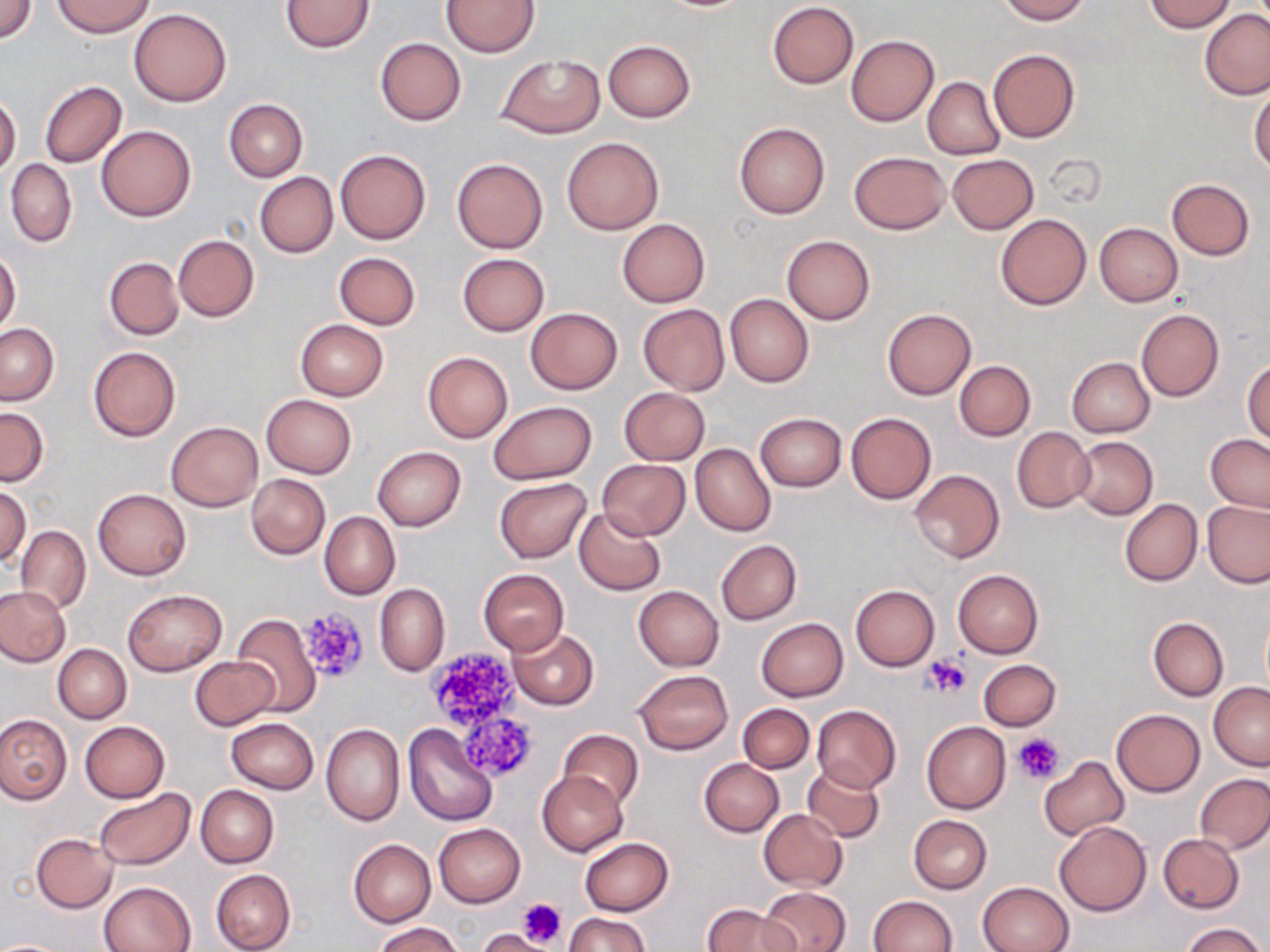

Approximate bounding boxes as (x1,y1)-(x2,y2) corner pairs in pixels. Uninfected red blood cell locations: (51,0)-(153,37), (280,0)-(376,53), (443,0)-(540,57), (998,0)-(1090,23), (1146,0)-(1234,32), (1,1)-(37,42), (768,2)-(858,88), (129,8)-(232,106), (1199,10)-(1270,100), (846,35)-(938,125), (375,38)-(465,125), (603,40)-(696,122), (988,49)-(1080,142), (496,54)-(605,137), (923,77)-(1005,160), (40,82)-(127,168), (1250,86)-(1269,178), (0,95)-(21,176), (224,98)-(308,182), (734,121)-(830,219), (96,125)-(195,221), (561,137)-(663,234), (336,148)-(431,244), (850,151)-(948,233), (947,154)-(1038,234), (451,158)-(548,254), (5,159)-(77,248), (254,172)-(338,258), (1167,179)-(1255,260), (995,212)-(1092,310), (617,219)-(710,308), (1094,223)-(1184,306), (172,234)-(260,322), (782,236)-(875,325), (0,250)-(21,335), (334,252)-(420,330), (457,253)-(549,335), (104,257)-(184,340), (724,293)-(814,387), (638,304)-(729,394), (526,307)-(622,395), (883,308)-(976,399), (1135,308)-(1224,402), (295,319)-(389,401), (0,323)-(58,405), (88,346)-(180,441), (423,351)-(513,443), (1067,357)-(1155,437), (1244,360)-(1270,445), (954,361)-(1035,441), (620,387)-(709,465), (613,389)-(699,539), (260,394)-(357,478), (490,400)-(597,483), (0,407)-(49,485), (755,412)-(846,491), (846,412)-(936,503), (166,421)-(262,511), (1011,428)-(1094,512), (1205,433)-(1270,512), (1071,436)-(1157,519), (690,443)-(776,536), (372,447)-(466,531), (596,458)-(691,540), (909,469)-(1004,564), (246,473)-(329,559), (495,477)-(592,562), (0,486)-(31,569), (93,489)-(191,580), (1119,499)-(1202,587), (1202,499)-(1270,588), (574,508)-(665,596), (319,511)-(400,600), (15,526)-(91,614), (715,540)-(802,625), (478,569)-(569,656), (952,570)-(1043,658), (374,583)-(449,676), (849,585)-(939,671), (0,586)-(71,667), (633,586)-(723,671), (123,590)-(227,676), (231,613)-(321,715), (1148,617)-(1228,701), (755,618)-(848,701), (509,629)-(599,709), (52,644)-(131,724), (189,656)-(279,731), (978,659)-(1061,730), (634,670)-(733,755), (1208,682)-(1270,771), (737,703)-(813,773), (812,704)-(900,793), (1110,709)-(1205,797), (0,712)-(72,805), (226,718)-(319,794), (80,720)-(169,802), (921,720)-(1011,813), (320,724)-(404,826), (404,724)-(497,824), (558,729)-(644,811), (1039,756)-(1129,840), (699,759)-(783,837), (802,763)-(884,842), (536,771)-(628,856), (1195,772)-(1270,855), (195,784)-(279,867), (92,788)-(195,870), (757,809)-(848,891), (908,814)-(992,894), (1053,820)-(1153,916), (434,823)-(525,908), (31,833)-(119,913), (1158,833)-(1244,913), (580,837)-(674,916), (348,839)-(436,928), (210,870)-(295,952), (98,881)-(195,952), (976,882)-(1075,952), (759,887)-(850,952), (869,896)-(958,952), (703,903)-(797,952), (565,912)-(651,952), (1181,922)-(1263,952), (373,923)-(464,952), (477,930)-(548,952), (0,940)-(69,952). Platelet locations: (297,607)-(370,682), (427,650)-(521,726), (923,654)-(972,698), (463,719)-(533,781), (1015,732)-(1065,783), (519,898)-(568,948), (475,929)-(549,952). Slide-level diagnosis: negative for blood parasites. Image is 1270×952 pixels. Thin blood film. One field of a larger specimen. 1000x magnification. Light microscopy. May-Grünwald-Giemsa stain.